Locate malaria parasites and leukocytes.
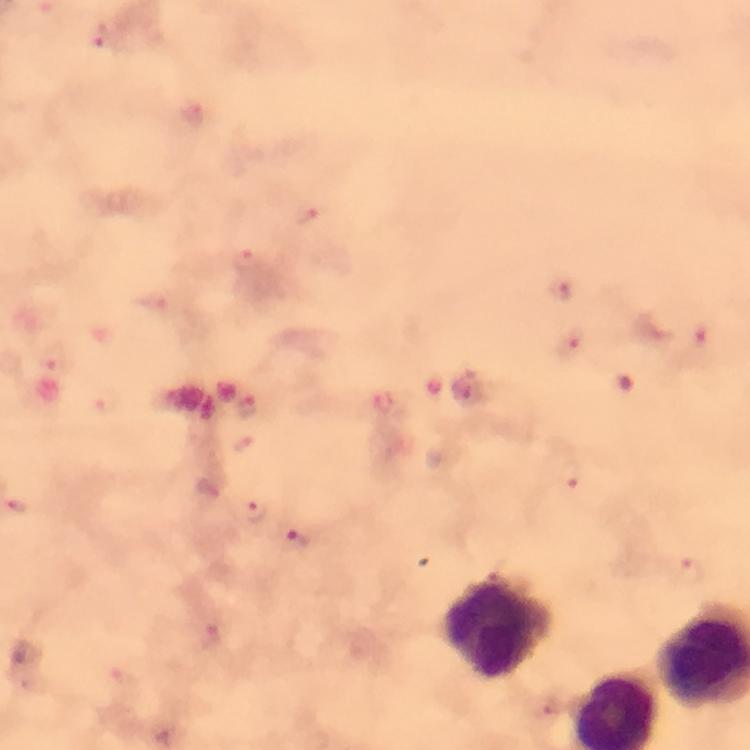

Approximate centers as [x, y] in pixels.
Malaria parasites: [99, 35], [192, 113], [310, 217], [247, 261], [562, 292], [568, 344], [253, 511], [296, 540], [208, 636].
Leukocytes: [497, 626].

Image is 750×750 pixels. Photographed through the microscope with a smartphone camera. Giemsa stain. 100x magnification. From a malaria diagnostic workup. Cropped region of a single field of view. Thick blood film. Immersion oil was used.